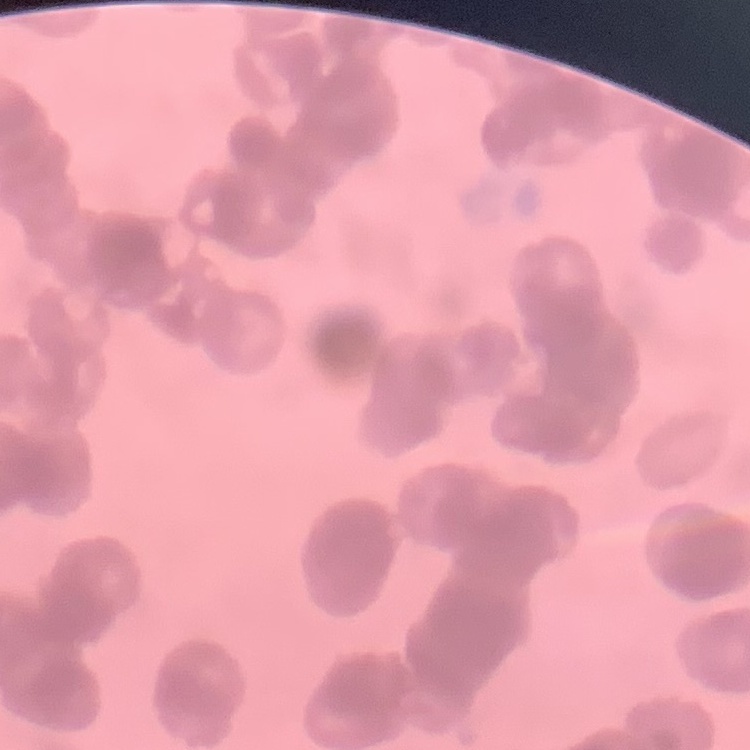
erythrocyte morphology = rouleaux formation
image type = one tile cut from a larger photomicrograph
stain = Field's or Giemsa
preparation = thin blood smear